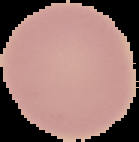
Summary:
  - Preparation: thin blood film
  - Image size: 139×142 pixels
  - Malaria status: uninfected
  - Image type: segmented cell region with the area outside set to black